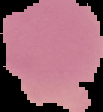
image size = 103×112 pixels
image type = segmented cell region with the area outside set to black
malaria status = uninfected
preparation = thin blood film